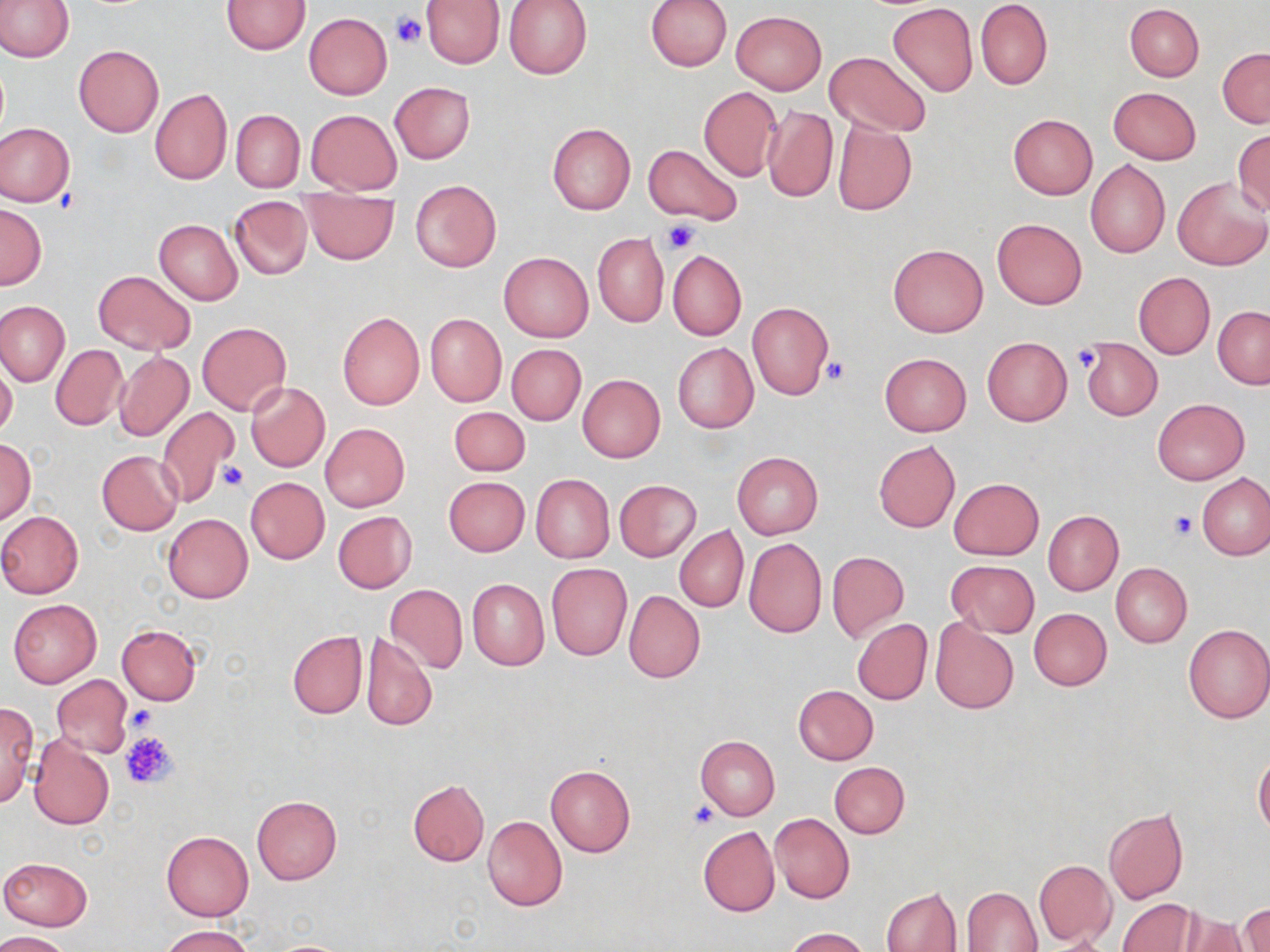

Summary:
  - Coordinate format: approximate bounding boxes as named x1/y1/x2/y2 corners in pixels
  - Platelet locations: (x1=391, y1=10, x2=426, y2=47), (x1=662, y1=220, x2=702, y2=253), (x1=1070, y1=346, x2=1101, y2=373), (x1=823, y1=356, x2=848, y2=385), (x1=219, y1=461, x2=247, y2=492), (x1=1170, y1=511, x2=1199, y2=539), (x1=125, y1=704, x2=158, y2=732), (x1=120, y1=730, x2=179, y2=787), (x1=688, y1=802, x2=718, y2=828)
  - Uninfected red blood cell locations: (x1=0, y1=0, x2=73, y2=63), (x1=422, y1=0, x2=504, y2=68), (x1=504, y1=0, x2=592, y2=79), (x1=645, y1=0, x2=732, y2=71), (x1=222, y1=1, x2=309, y2=54), (x1=976, y1=1, x2=1052, y2=89), (x1=887, y1=3, x2=978, y2=97), (x1=1124, y1=4, x2=1205, y2=81), (x1=730, y1=10, x2=827, y2=95), (x1=304, y1=13, x2=393, y2=99), (x1=73, y1=45, x2=163, y2=137), (x1=1218, y1=48, x2=1270, y2=128), (x1=823, y1=52, x2=931, y2=136), (x1=389, y1=81, x2=476, y2=163), (x1=698, y1=86, x2=782, y2=182), (x1=1108, y1=87, x2=1201, y2=164), (x1=149, y1=88, x2=232, y2=184), (x1=764, y1=105, x2=838, y2=202), (x1=306, y1=109, x2=401, y2=195), (x1=231, y1=110, x2=303, y2=191), (x1=1008, y1=114, x2=1097, y2=199), (x1=832, y1=117, x2=917, y2=216), (x1=0, y1=122, x2=74, y2=206), (x1=547, y1=123, x2=635, y2=215), (x1=1232, y1=130, x2=1270, y2=215), (x1=643, y1=143, x2=743, y2=227), (x1=1085, y1=160, x2=1170, y2=258), (x1=1174, y1=176, x2=1270, y2=270), (x1=410, y1=182, x2=501, y2=272), (x1=301, y1=193, x2=398, y2=264), (x1=229, y1=196, x2=313, y2=279), (x1=0, y1=203, x2=46, y2=290), (x1=992, y1=217, x2=1088, y2=310), (x1=154, y1=218, x2=243, y2=305), (x1=592, y1=233, x2=669, y2=327), (x1=888, y1=243, x2=987, y2=336), (x1=667, y1=249, x2=747, y2=340), (x1=498, y1=251, x2=593, y2=342), (x1=93, y1=270, x2=196, y2=355), (x1=1133, y1=273, x2=1216, y2=359), (x1=0, y1=301, x2=71, y2=386), (x1=747, y1=302, x2=834, y2=399), (x1=1213, y1=307, x2=1270, y2=388), (x1=337, y1=312, x2=425, y2=410), (x1=425, y1=313, x2=507, y2=407), (x1=197, y1=322, x2=291, y2=415), (x1=982, y1=337, x2=1071, y2=425), (x1=1081, y1=338, x2=1162, y2=420), (x1=672, y1=341, x2=759, y2=433), (x1=51, y1=344, x2=129, y2=430), (x1=506, y1=344, x2=586, y2=425), (x1=115, y1=352, x2=193, y2=441), (x1=879, y1=352, x2=971, y2=437), (x1=0, y1=363, x2=17, y2=439), (x1=577, y1=374, x2=665, y2=462), (x1=246, y1=382, x2=330, y2=471), (x1=1152, y1=398, x2=1250, y2=484), (x1=155, y1=406, x2=240, y2=506), (x1=449, y1=406, x2=529, y2=475), (x1=320, y1=423, x2=409, y2=512), (x1=0, y1=440, x2=36, y2=523), (x1=873, y1=440, x2=960, y2=532), (x1=97, y1=450, x2=183, y2=535), (x1=732, y1=452, x2=823, y2=539), (x1=1197, y1=473, x2=1269, y2=561), (x1=530, y1=474, x2=614, y2=563), (x1=443, y1=476, x2=530, y2=556), (x1=245, y1=477, x2=329, y2=563), (x1=949, y1=478, x2=1043, y2=560), (x1=614, y1=480, x2=702, y2=562), (x1=1044, y1=510, x2=1123, y2=595), (x1=0, y1=511, x2=84, y2=599), (x1=333, y1=511, x2=416, y2=593), (x1=163, y1=513, x2=253, y2=603), (x1=674, y1=527, x2=747, y2=612), (x1=743, y1=538, x2=827, y2=639), (x1=827, y1=550, x2=909, y2=643), (x1=945, y1=560, x2=1039, y2=638), (x1=546, y1=563, x2=633, y2=661), (x1=1111, y1=563, x2=1192, y2=648), (x1=467, y1=578, x2=549, y2=670), (x1=384, y1=584, x2=467, y2=674), (x1=624, y1=592, x2=705, y2=682), (x1=8, y1=598, x2=102, y2=689), (x1=1028, y1=607, x2=1111, y2=691), (x1=851, y1=618, x2=932, y2=705), (x1=930, y1=619, x2=1019, y2=715), (x1=1182, y1=622, x2=1270, y2=723), (x1=116, y1=624, x2=202, y2=705), (x1=287, y1=630, x2=368, y2=718), (x1=360, y1=633, x2=437, y2=732), (x1=52, y1=675, x2=133, y2=758), (x1=792, y1=684, x2=878, y2=765), (x1=0, y1=701, x2=38, y2=807), (x1=27, y1=734, x2=115, y2=830), (x1=695, y1=735, x2=779, y2=821), (x1=1253, y1=755, x2=1270, y2=836), (x1=829, y1=762, x2=910, y2=838), (x1=545, y1=765, x2=635, y2=859), (x1=408, y1=779, x2=489, y2=866), (x1=251, y1=795, x2=343, y2=885), (x1=1103, y1=808, x2=1188, y2=904), (x1=770, y1=813, x2=854, y2=903), (x1=482, y1=815, x2=568, y2=911), (x1=698, y1=826, x2=779, y2=917), (x1=162, y1=830, x2=253, y2=921), (x1=0, y1=856, x2=92, y2=931), (x1=1033, y1=858, x2=1116, y2=947), (x1=962, y1=876, x2=1113, y2=949), (x1=881, y1=887, x2=963, y2=952), (x1=961, y1=887, x2=1041, y2=952), (x1=1118, y1=898, x2=1197, y2=952), (x1=1239, y1=903, x2=1269, y2=952), (x1=1179, y1=912, x2=1252, y2=952), (x1=162, y1=926, x2=253, y2=952), (x1=784, y1=927, x2=870, y2=952), (x1=0, y1=930, x2=72, y2=952), (x1=263, y1=938, x2=359, y2=951)
  - Slide-level diagnosis: negative for blood parasites
  - Magnification: 1000x
  - Field of view: single
  - Preparation: thin blood smear
  - Stain: May-Grünwald-Giemsa
  - Modality: light microscopy
  - Image size: 1270×952 pixels